Locate every Plasmodium falciparum-infected red blood cell.
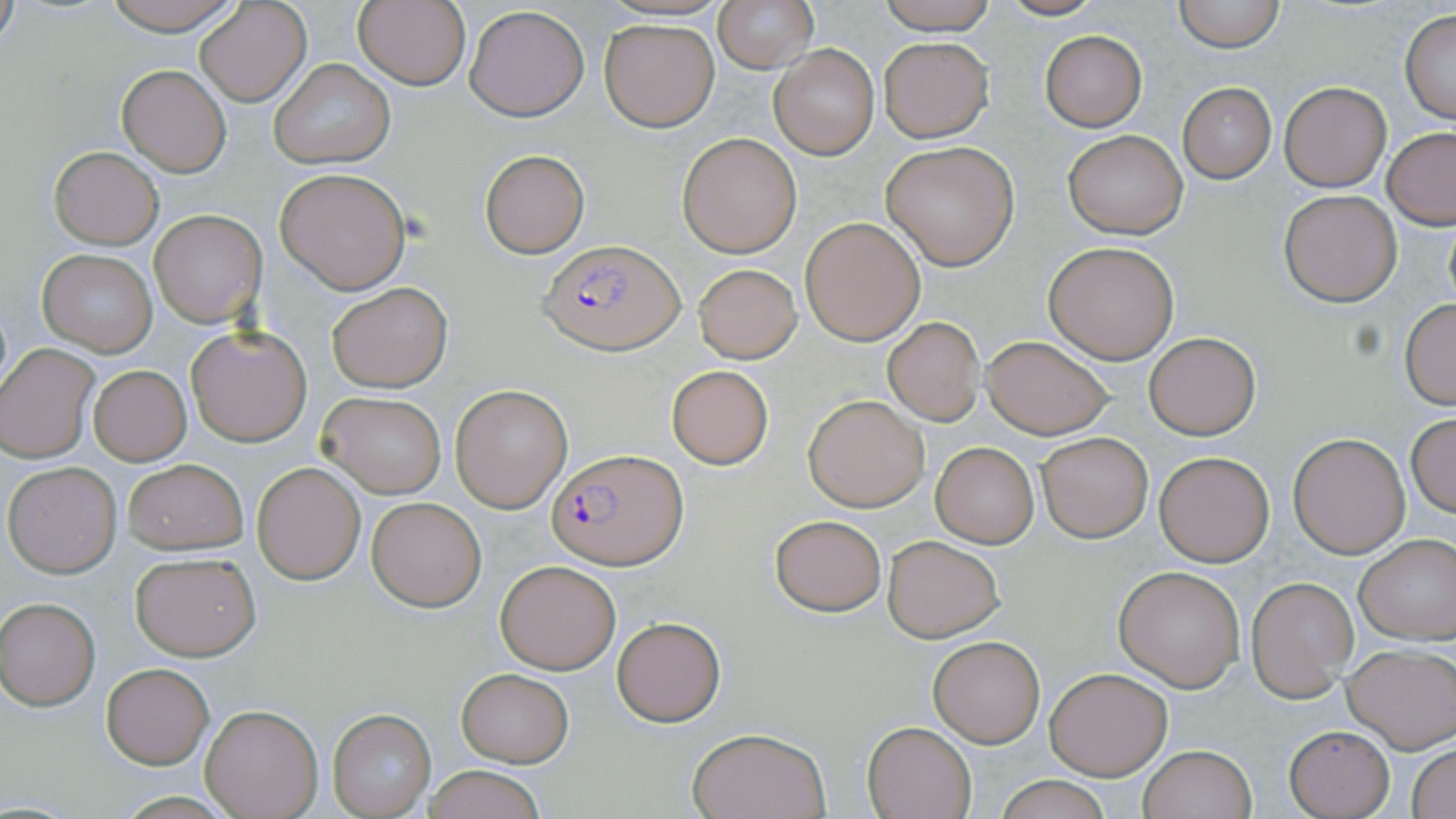
Approximate bounding boxes as named x1/y1/x2/y2 corners in pixels.
Plasmodium falciparum-infected red blood cells: (x1=540, y1=240, x2=683, y2=354), (x1=547, y1=449, x2=687, y2=570).

Summary:
  - Uninfected red blood cell locations: (x1=96, y1=0, x2=248, y2=34), (x1=195, y1=0, x2=311, y2=107), (x1=352, y1=0, x2=471, y2=91), (x1=714, y1=0, x2=818, y2=73), (x1=874, y1=0, x2=999, y2=34), (x1=994, y1=0, x2=1109, y2=21), (x1=1172, y1=0, x2=1287, y2=52), (x1=1, y1=3, x2=19, y2=53), (x1=465, y1=5, x2=589, y2=122), (x1=1399, y1=10, x2=1456, y2=124), (x1=600, y1=19, x2=719, y2=131), (x1=1041, y1=31, x2=1148, y2=130), (x1=880, y1=37, x2=992, y2=141), (x1=771, y1=45, x2=879, y2=158), (x1=271, y1=58, x2=395, y2=168), (x1=118, y1=66, x2=230, y2=176), (x1=1280, y1=82, x2=1389, y2=191), (x1=1177, y1=83, x2=1276, y2=184), (x1=1382, y1=128, x2=1456, y2=230), (x1=1063, y1=130, x2=1187, y2=240), (x1=677, y1=133, x2=801, y2=258), (x1=881, y1=141, x2=1020, y2=270), (x1=49, y1=146, x2=163, y2=249), (x1=479, y1=149, x2=589, y2=257), (x1=274, y1=167, x2=411, y2=294), (x1=1279, y1=191, x2=1400, y2=307), (x1=150, y1=210, x2=267, y2=328), (x1=1442, y1=210, x2=1456, y2=315), (x1=799, y1=218, x2=925, y2=345), (x1=1044, y1=240, x2=1179, y2=363), (x1=38, y1=250, x2=157, y2=355), (x1=694, y1=262, x2=801, y2=363), (x1=327, y1=282, x2=454, y2=392), (x1=1400, y1=299, x2=1456, y2=410), (x1=883, y1=318, x2=984, y2=426), (x1=186, y1=324, x2=312, y2=447), (x1=1143, y1=331, x2=1261, y2=441), (x1=980, y1=335, x2=1114, y2=439), (x1=1, y1=345, x2=98, y2=462), (x1=88, y1=365, x2=191, y2=465), (x1=666, y1=365, x2=773, y2=468), (x1=451, y1=386, x2=572, y2=513), (x1=317, y1=392, x2=447, y2=497), (x1=803, y1=395, x2=929, y2=512), (x1=1406, y1=414, x2=1456, y2=520), (x1=1036, y1=431, x2=1153, y2=542), (x1=1288, y1=432, x2=1410, y2=558), (x1=930, y1=441, x2=1039, y2=548), (x1=1153, y1=451, x2=1273, y2=566), (x1=122, y1=458, x2=247, y2=556), (x1=4, y1=462, x2=122, y2=577), (x1=253, y1=462, x2=365, y2=584), (x1=368, y1=497, x2=487, y2=611), (x1=770, y1=515, x2=887, y2=615), (x1=881, y1=534, x2=1005, y2=642), (x1=1355, y1=536, x2=1456, y2=644), (x1=130, y1=551, x2=262, y2=661), (x1=495, y1=559, x2=619, y2=673), (x1=1114, y1=566, x2=1245, y2=691), (x1=1248, y1=579, x2=1357, y2=702), (x1=1, y1=598, x2=99, y2=710), (x1=612, y1=616, x2=725, y2=726), (x1=927, y1=635, x2=1045, y2=747), (x1=1343, y1=645, x2=1456, y2=752), (x1=101, y1=662, x2=214, y2=768), (x1=1045, y1=666, x2=1171, y2=779), (x1=456, y1=668, x2=573, y2=768), (x1=199, y1=704, x2=323, y2=819), (x1=329, y1=710, x2=435, y2=818), (x1=862, y1=720, x2=978, y2=819), (x1=1284, y1=726, x2=1394, y2=818), (x1=686, y1=727, x2=830, y2=819), (x1=1408, y1=744, x2=1456, y2=819), (x1=1138, y1=745, x2=1256, y2=819), (x1=422, y1=765, x2=548, y2=819), (x1=990, y1=775, x2=1118, y2=819)
  - Slide-level diagnosis: Plasmodium falciparum
  - Preparation: thin blood smear
  - Image size: 1456×819 pixels
  - Stain: May-Grünwald-Giemsa
  - Field of view: single
  - Modality: optical microscopy
  - Magnification: 1000x